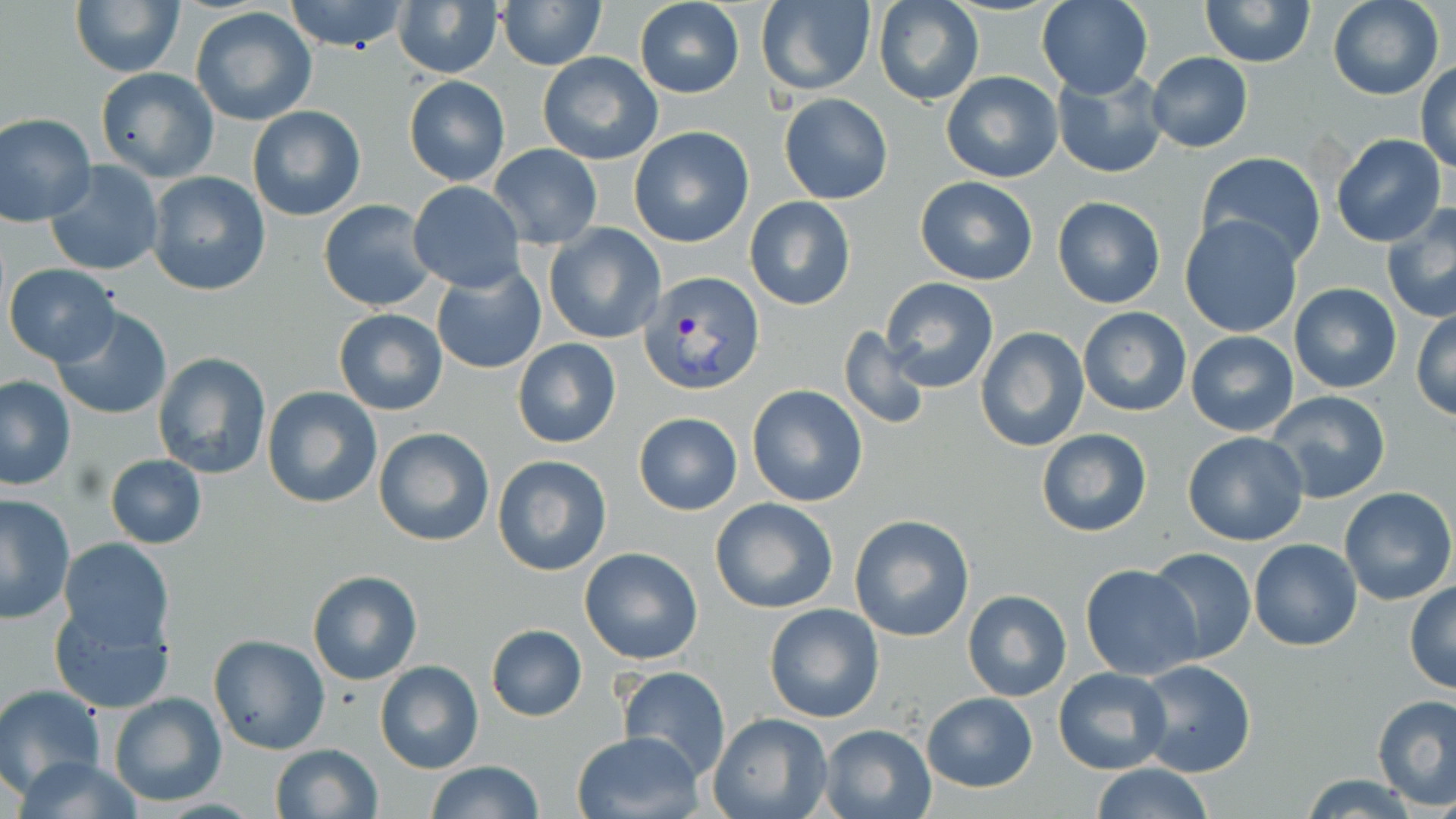
slide_level_diagnosis: Plasmodium vivax
modality: optical microscopy
magnification: 1000x
plasmodium_vivax_infected_red_blood_cell_locations: 'approximate bounding boxes as named x1/y1/x2/y2 corners in pixels: (x1=636, y1=269, x2=761, y2=394)'
stain: May-Grünwald-Giemsa
uninfected_red_blood_cell_locations: 'approximate bounding boxes as named x1/y1/x2/y2 corners in pixels: (x1=69, y1=0, x2=185, y2=77), (x1=284, y1=0, x2=409, y2=53), (x1=496, y1=0, x2=606, y2=71), (x1=1037, y1=0, x2=1152, y2=99), (x1=1200, y1=0, x2=1316, y2=67), (x1=1328, y1=0, x2=1443, y2=101), (x1=756, y1=1, x2=876, y2=96), (x1=873, y1=1, x2=984, y2=106), (x1=635, y1=2, x2=745, y2=98), (x1=394, y1=3, x2=502, y2=78), (x1=190, y1=7, x2=317, y2=126), (x1=537, y1=51, x2=663, y2=165), (x1=1146, y1=52, x2=1253, y2=152), (x1=1415, y1=64, x2=1456, y2=174), (x1=95, y1=68, x2=219, y2=183), (x1=1053, y1=68, x2=1167, y2=179), (x1=941, y1=71, x2=1063, y2=183), (x1=404, y1=75, x2=510, y2=185), (x1=779, y1=92, x2=893, y2=205), (x1=247, y1=105, x2=365, y2=221), (x1=0, y1=112, x2=97, y2=226), (x1=628, y1=126, x2=755, y2=247), (x1=1331, y1=133, x2=1447, y2=246), (x1=489, y1=144, x2=601, y2=249), (x1=1197, y1=153, x2=1326, y2=269), (x1=44, y1=161, x2=163, y2=278), (x1=146, y1=171, x2=270, y2=296), (x1=914, y1=176, x2=1039, y2=285), (x1=409, y1=182, x2=524, y2=292), (x1=744, y1=195, x2=857, y2=311), (x1=1051, y1=196, x2=1167, y2=308), (x1=317, y1=199, x2=439, y2=311), (x1=1380, y1=205, x2=1456, y2=323), (x1=1178, y1=214, x2=1304, y2=339), (x1=544, y1=224, x2=665, y2=344), (x1=4, y1=264, x2=118, y2=366), (x1=432, y1=265, x2=546, y2=375), (x1=879, y1=277, x2=999, y2=394), (x1=1288, y1=283, x2=1402, y2=395), (x1=50, y1=306, x2=173, y2=421), (x1=1078, y1=307, x2=1191, y2=417), (x1=1411, y1=307, x2=1456, y2=421), (x1=333, y1=309, x2=447, y2=415), (x1=838, y1=325, x2=931, y2=430), (x1=975, y1=327, x2=1088, y2=450), (x1=1186, y1=330, x2=1298, y2=437), (x1=513, y1=339, x2=621, y2=449), (x1=153, y1=352, x2=272, y2=479), (x1=0, y1=377, x2=75, y2=490), (x1=746, y1=384, x2=868, y2=506), (x1=262, y1=385, x2=383, y2=511), (x1=1265, y1=390, x2=1392, y2=502), (x1=633, y1=412, x2=742, y2=515), (x1=373, y1=425, x2=495, y2=548), (x1=1035, y1=427, x2=1152, y2=537), (x1=1181, y1=430, x2=1310, y2=547), (x1=492, y1=454, x2=612, y2=576), (x1=104, y1=455, x2=207, y2=548), (x1=1339, y1=486, x2=1455, y2=605), (x1=0, y1=494, x2=74, y2=625), (x1=709, y1=497, x2=840, y2=615), (x1=849, y1=514, x2=975, y2=642), (x1=59, y1=538, x2=173, y2=651), (x1=1249, y1=539, x2=1362, y2=652), (x1=579, y1=547, x2=704, y2=665), (x1=1145, y1=547, x2=1257, y2=665), (x1=1079, y1=564, x2=1202, y2=681), (x1=306, y1=569, x2=426, y2=687), (x1=1404, y1=582, x2=1456, y2=694), (x1=962, y1=589, x2=1071, y2=702), (x1=51, y1=601, x2=175, y2=714), (x1=764, y1=602, x2=885, y2=723), (x1=486, y1=624, x2=587, y2=722), (x1=207, y1=636, x2=330, y2=755), (x1=1133, y1=659, x2=1257, y2=780), (x1=374, y1=660, x2=484, y2=775), (x1=617, y1=665, x2=731, y2=780), (x1=1054, y1=667, x2=1171, y2=775), (x1=0, y1=684, x2=104, y2=795), (x1=920, y1=691, x2=1038, y2=793), (x1=107, y1=692, x2=226, y2=806), (x1=1372, y1=694, x2=1455, y2=809), (x1=708, y1=711, x2=834, y2=819), (x1=820, y1=713, x2=1032, y2=807), (x1=818, y1=725, x2=936, y2=819), (x1=572, y1=730, x2=703, y2=818), (x1=269, y1=744, x2=382, y2=819), (x1=12, y1=756, x2=147, y2=817), (x1=424, y1=760, x2=545, y2=819), (x1=1088, y1=763, x2=1215, y2=819), (x1=1300, y1=774, x2=1422, y2=818)'
image_size: 1456×819 pixels
field_of_view: single
preparation: thin blood smear